Give the extent of all Plasmodium ovale-infected red blood cells.
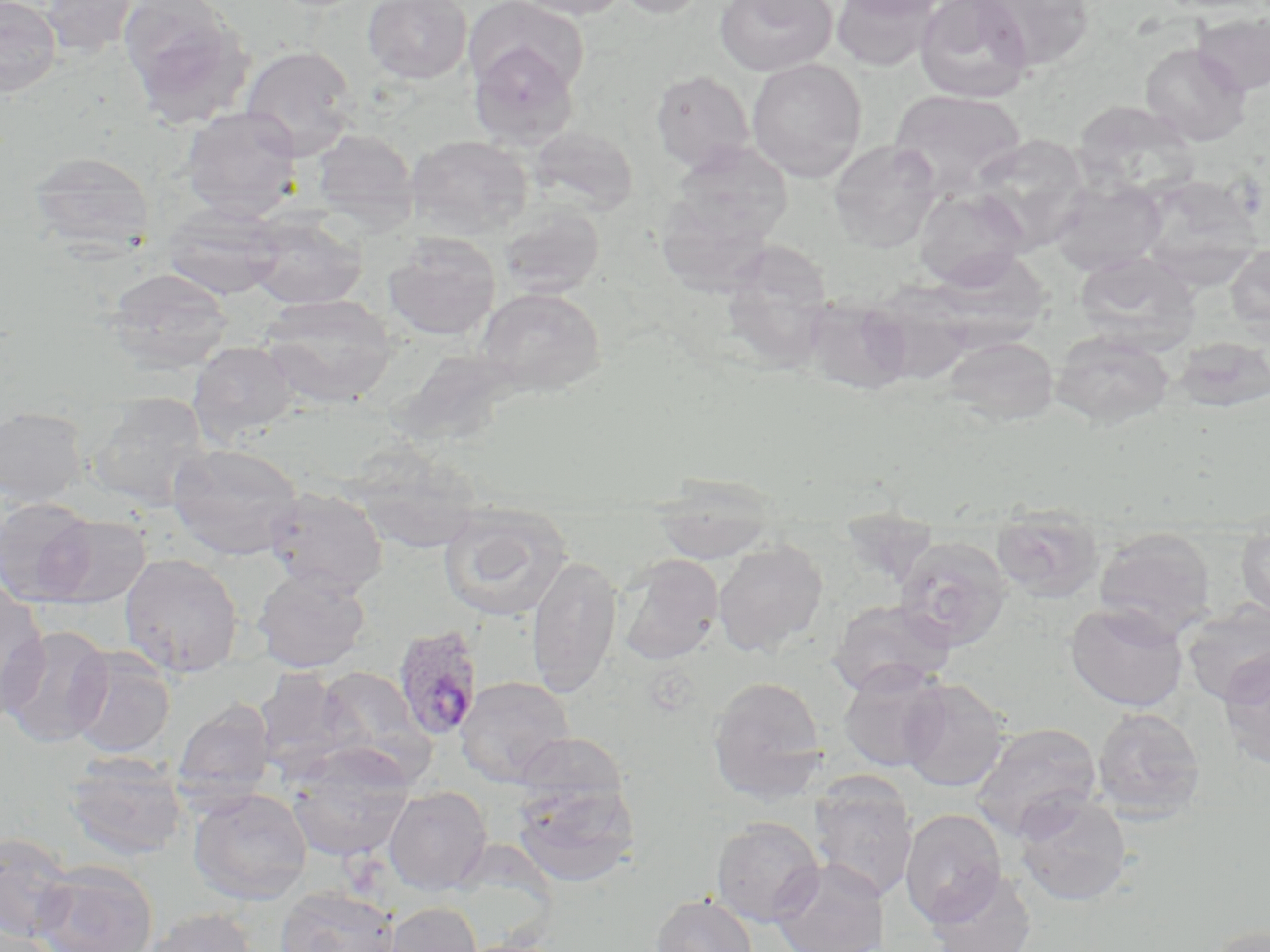
Approximate bounding boxes as (x1, y1, x2, y2) in pixels.
Plasmodium ovale-infected red blood cells: (392, 625, 484, 742).

{
  "slide_level_diagnosis": "Plasmodium ovale",
  "uninfected_red_blood_cell_locations": "approximate bounding boxes as (x1, y1, x2, y2) in pixels: (40, 0, 142, 59), (117, 0, 253, 125), (363, 0, 472, 84), (513, 0, 634, 20), (610, 0, 712, 19), (715, 0, 837, 76), (831, 0, 942, 71), (836, 0, 951, 18), (914, 0, 1035, 104), (974, 0, 1095, 70), (1155, 0, 1268, 16), (0, 1, 63, 97), (465, 1, 589, 96), (1192, 11, 1270, 96), (467, 42, 580, 148), (1140, 43, 1251, 146), (239, 45, 359, 159), (746, 58, 868, 183), (650, 70, 755, 172), (889, 89, 1026, 197), (1073, 100, 1199, 199), (180, 106, 304, 222), (528, 125, 639, 216), (311, 129, 419, 231), (406, 134, 533, 239), (970, 134, 1091, 251), (828, 140, 942, 252), (667, 142, 794, 248), (27, 151, 155, 257), (1136, 174, 1264, 285), (1050, 177, 1167, 276), (914, 187, 1029, 291), (497, 201, 605, 299), (162, 203, 286, 301), (243, 212, 367, 310), (383, 234, 501, 341), (720, 243, 836, 367), (1225, 243, 1270, 341), (938, 249, 1045, 359), (1075, 251, 1199, 355), (103, 266, 234, 374), (476, 287, 606, 397), (258, 293, 398, 407), (801, 294, 914, 396), (1051, 329, 1174, 430), (942, 336, 1059, 427), (1173, 336, 1270, 413), (189, 341, 299, 446), (401, 353, 506, 451), (87, 392, 212, 511), (0, 407, 89, 507), (167, 442, 305, 560), (344, 443, 487, 554), (649, 481, 780, 567), (262, 486, 389, 598), (0, 497, 98, 605), (437, 504, 573, 622), (991, 504, 1105, 603), (41, 514, 151, 608), (1235, 521, 1270, 621), (1093, 526, 1216, 641), (892, 535, 1013, 651), (713, 540, 828, 656), (119, 553, 243, 679), (618, 554, 724, 664), (526, 555, 623, 697), (252, 569, 371, 673), (0, 581, 51, 719), (828, 599, 954, 697), (1181, 600, 1270, 705), (1065, 601, 1188, 712), (1, 625, 113, 749), (68, 646, 176, 759), (1217, 651, 1270, 769), (838, 662, 950, 772), (315, 666, 431, 776), (253, 669, 358, 778), (707, 675, 827, 804), (455, 676, 575, 787), (898, 678, 1010, 792), (173, 699, 276, 806), (1091, 706, 1206, 822), (970, 722, 1103, 840), (513, 731, 632, 816), (286, 745, 414, 862), (64, 751, 190, 861), (808, 773, 919, 904), (511, 779, 640, 888), (384, 786, 492, 895), (187, 787, 313, 906), (1013, 792, 1133, 908), (899, 808, 1008, 927), (711, 816, 824, 926), (0, 832, 77, 945), (769, 858, 889, 952), (32, 861, 158, 952), (926, 868, 1038, 952), (274, 886, 401, 952), (651, 893, 757, 952), (382, 902, 483, 952), (141, 907, 259, 952), (1, 915, 55, 951), (1201, 924, 1270, 952)",
  "image_size": "1270×952 pixels",
  "modality": "light microscopy",
  "magnification": "1000x",
  "preparation": "thin blood film",
  "stain": "May-Grünwald-Giemsa",
  "field_of_view": "single"
}